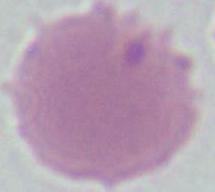
{
  "modality": "micrograph",
  "magnification": "1000x",
  "identification": "red blood cell"
}